Classify this cell by malaria status.
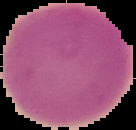

Uninfected.

Image is 136×130 pixels. Cell region segmented out of the field of view; the surrounding area is masked to black. From a thin blood smear.